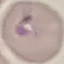
Summary:
  - Malaria status: parasitized
  - Image type: cell patch, automatically extracted from a larger field of view and resized to 64 × 64 pixels
  - Preparation: thin blood film
  - Capture: smartphone through the microscope eyepiece
  - Stain: Giemsa